State the blood parasite species.
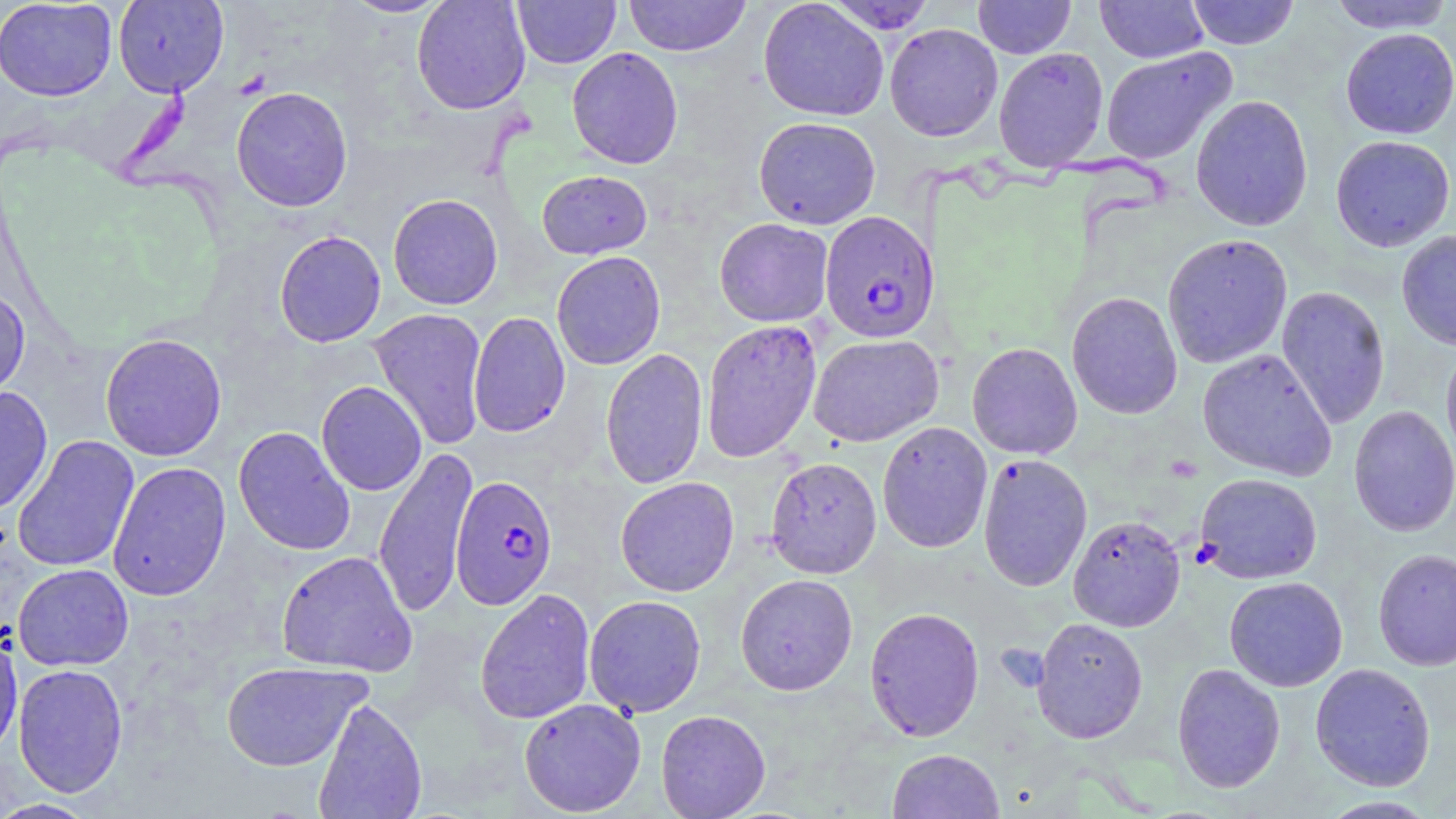
Plasmodium falciparum.

Approximate bounding boxes as [x1, y1, x2, y2] in pixels. Uninfected red blood cell locations: [0, 0, 117, 101], [112, 0, 229, 98], [341, 0, 450, 18], [411, 0, 531, 114], [512, 0, 621, 69], [624, 0, 751, 57], [757, 0, 889, 122], [973, 0, 1076, 58], [1095, 0, 1209, 63], [1186, 0, 1300, 50], [1327, 0, 1454, 34], [824, 1, 938, 34], [884, 23, 1003, 141], [1340, 28, 1456, 140], [566, 46, 684, 169], [1100, 46, 1237, 165], [993, 47, 1109, 171], [231, 86, 353, 212], [1190, 94, 1313, 231], [753, 116, 881, 229], [1330, 135, 1455, 251], [537, 170, 652, 259], [388, 193, 503, 310], [714, 218, 833, 327], [1396, 229, 1456, 350], [274, 230, 386, 347], [1162, 233, 1293, 369], [551, 251, 666, 370], [0, 284, 31, 402], [1276, 285, 1390, 430], [1066, 292, 1183, 419], [368, 307, 488, 450], [468, 312, 570, 437], [701, 319, 822, 463], [100, 333, 227, 461], [808, 333, 943, 447], [967, 342, 1082, 459], [1441, 342, 1456, 470], [600, 347, 708, 489], [1197, 348, 1337, 481], [316, 381, 427, 496], [0, 386, 53, 515], [1349, 405, 1456, 537], [877, 421, 993, 553], [233, 426, 355, 556], [12, 436, 139, 573], [374, 446, 478, 619], [978, 453, 1093, 592], [766, 456, 882, 578], [107, 461, 232, 602], [1195, 472, 1323, 584], [615, 476, 739, 597], [1068, 514, 1186, 632], [1373, 548, 1456, 671], [276, 550, 417, 677], [13, 563, 134, 671], [735, 574, 858, 695], [1224, 576, 1348, 692], [475, 587, 596, 725], [584, 594, 706, 717], [864, 607, 985, 742], [1031, 617, 1148, 743], [0, 629, 22, 760], [221, 661, 370, 771], [13, 663, 129, 797], [1172, 663, 1286, 793], [1310, 663, 1436, 791], [313, 697, 427, 819], [518, 698, 646, 816], [655, 709, 771, 819], [886, 748, 1005, 818], [1314, 795, 1443, 818], [0, 798, 100, 818]. Plasmodium falciparum-infected red blood cell locations: [819, 210, 939, 343], [451, 475, 557, 609]. May-Grünwald-Giemsa-stained preparation. Captured at 1000x magnification. Optical microscopy. Thin blood film. Image is 1456×819 pixels. Single field of view.